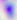
{
  "identification": "Toxoplasma gondii",
  "modality": "photomicrograph",
  "magnification": "400x"
}